State which parasite is depicted.
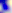

This is Toxoplasma gondii.

magnification = 400x
modality = photomicrograph